Assess this cell for malaria.
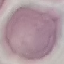
Uninfected.

capture = smartphone through the microscope eyepiece
image type = automatically extracted cell patch, resized to 64 × 64 pixels
stain = Giemsa
preparation = thin blood film